State which parasite is depicted.
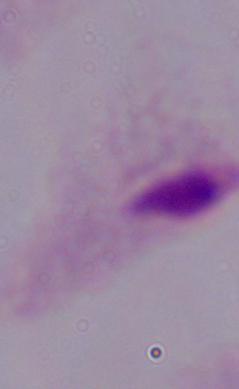

This is a trichomonad.

modality = micrograph
magnification = 1000x